Locate platelets.
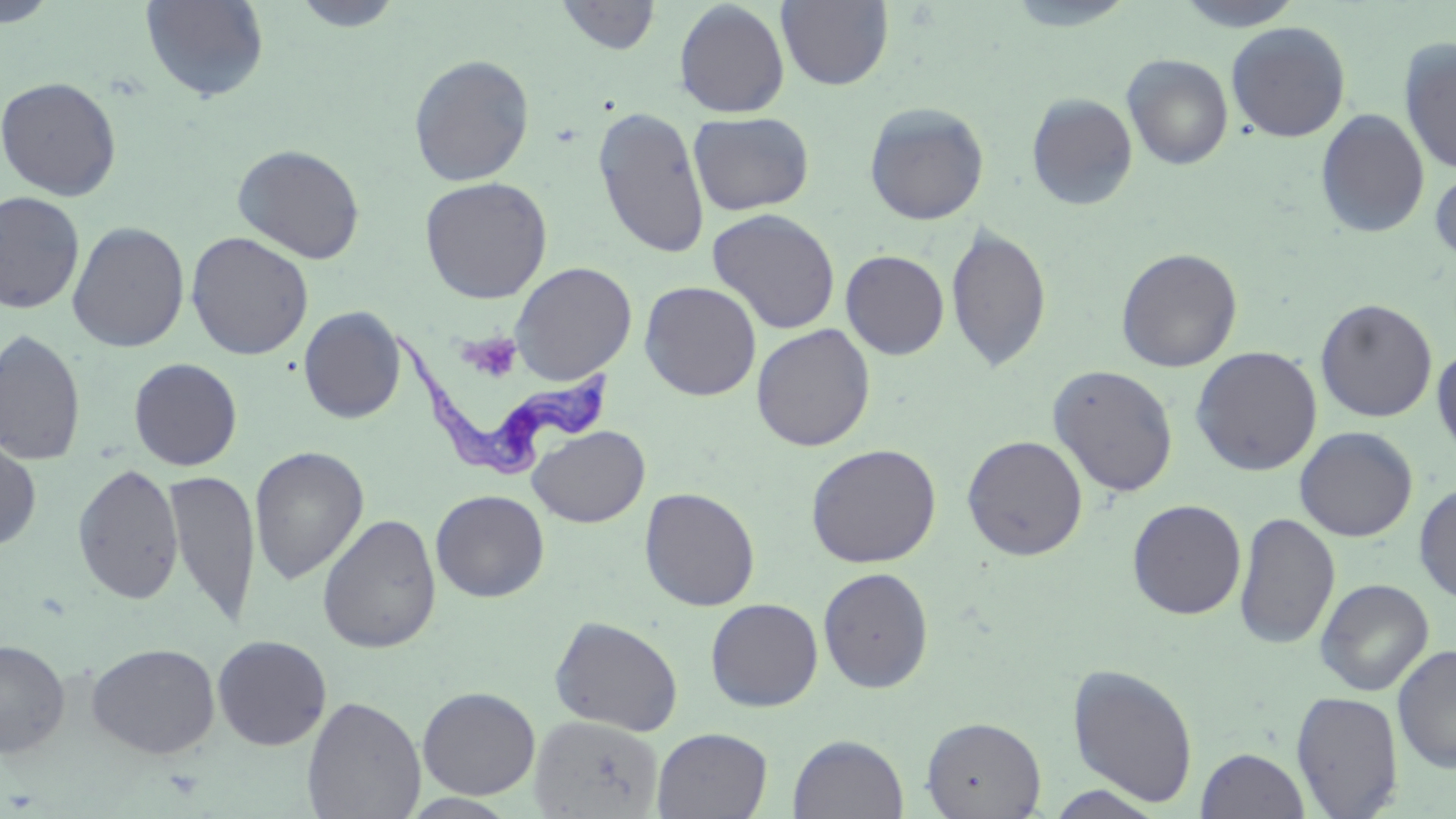
Approximate bounding boxes as named x1/y1/x2/y2 corners in pixels.
Platelets: (x1=462, y1=332, x2=524, y2=381).

slide-level diagnosis = Trypanosoma brucei
stain = May-Grünwald-Giemsa
image size = 1456×819 pixels
modality = optical microscopy
preparation = thin blood smear
field of view = one of a larger specimen
Trypanosoma brucei locations = approximate bounding boxes as named x1/y1/x2/y2 corners in pixels: (x1=388, y1=329, x2=611, y2=480)
magnification = 1000x
uninfected red blood cell locations = approximate bounding boxes as named x1/y1/x2/y2 corners in pixels: (x1=140, y1=0, x2=269, y2=103), (x1=288, y1=0, x2=406, y2=32), (x1=555, y1=0, x2=662, y2=55), (x1=775, y1=0, x2=893, y2=91), (x1=1172, y1=0, x2=1306, y2=31), (x1=0, y1=1, x2=61, y2=28), (x1=673, y1=1, x2=790, y2=118), (x1=1000, y1=2, x2=1141, y2=31), (x1=1226, y1=21, x2=1351, y2=142), (x1=1398, y1=37, x2=1456, y2=175), (x1=408, y1=54, x2=535, y2=186), (x1=1122, y1=54, x2=1234, y2=170), (x1=0, y1=75, x2=122, y2=200), (x1=1026, y1=93, x2=1139, y2=211), (x1=863, y1=101, x2=989, y2=225), (x1=593, y1=106, x2=710, y2=259), (x1=1315, y1=108, x2=1430, y2=239), (x1=689, y1=111, x2=813, y2=215), (x1=232, y1=143, x2=366, y2=264), (x1=1430, y1=164, x2=1456, y2=267), (x1=419, y1=176, x2=553, y2=304), (x1=0, y1=191, x2=85, y2=315), (x1=707, y1=208, x2=841, y2=335), (x1=67, y1=221, x2=190, y2=352), (x1=945, y1=223, x2=1052, y2=374), (x1=186, y1=232, x2=314, y2=360), (x1=1116, y1=247, x2=1243, y2=372), (x1=840, y1=249, x2=950, y2=360), (x1=510, y1=262, x2=638, y2=384), (x1=639, y1=280, x2=762, y2=401), (x1=1315, y1=298, x2=1438, y2=422), (x1=298, y1=306, x2=406, y2=424), (x1=751, y1=323, x2=875, y2=451), (x1=0, y1=328, x2=86, y2=467), (x1=1431, y1=344, x2=1456, y2=459), (x1=1191, y1=346, x2=1323, y2=476), (x1=128, y1=357, x2=243, y2=471), (x1=1047, y1=364, x2=1179, y2=498), (x1=528, y1=425, x2=650, y2=527), (x1=1294, y1=426, x2=1418, y2=541), (x1=0, y1=433, x2=42, y2=553), (x1=962, y1=435, x2=1088, y2=561), (x1=805, y1=443, x2=942, y2=568), (x1=249, y1=446, x2=369, y2=584), (x1=73, y1=463, x2=184, y2=605), (x1=163, y1=469, x2=260, y2=628), (x1=1414, y1=482, x2=1456, y2=603), (x1=639, y1=487, x2=760, y2=611), (x1=430, y1=489, x2=550, y2=602), (x1=1127, y1=499, x2=1247, y2=620), (x1=1234, y1=512, x2=1341, y2=650), (x1=317, y1=513, x2=442, y2=654), (x1=818, y1=567, x2=934, y2=693), (x1=1315, y1=578, x2=1433, y2=696), (x1=705, y1=597, x2=823, y2=712), (x1=549, y1=615, x2=684, y2=736), (x1=212, y1=634, x2=332, y2=750), (x1=0, y1=639, x2=71, y2=758), (x1=87, y1=642, x2=221, y2=759), (x1=1393, y1=644, x2=1456, y2=774), (x1=1066, y1=663, x2=1199, y2=807), (x1=417, y1=686, x2=541, y2=800), (x1=1291, y1=691, x2=1403, y2=818), (x1=302, y1=695, x2=426, y2=819), (x1=528, y1=715, x2=664, y2=818), (x1=921, y1=716, x2=1046, y2=819), (x1=651, y1=727, x2=773, y2=819), (x1=787, y1=734, x2=910, y2=818), (x1=1196, y1=747, x2=1310, y2=819), (x1=1040, y1=784, x2=1168, y2=818), (x1=400, y1=793, x2=522, y2=817)